Locate every blood parasite and identify its species.
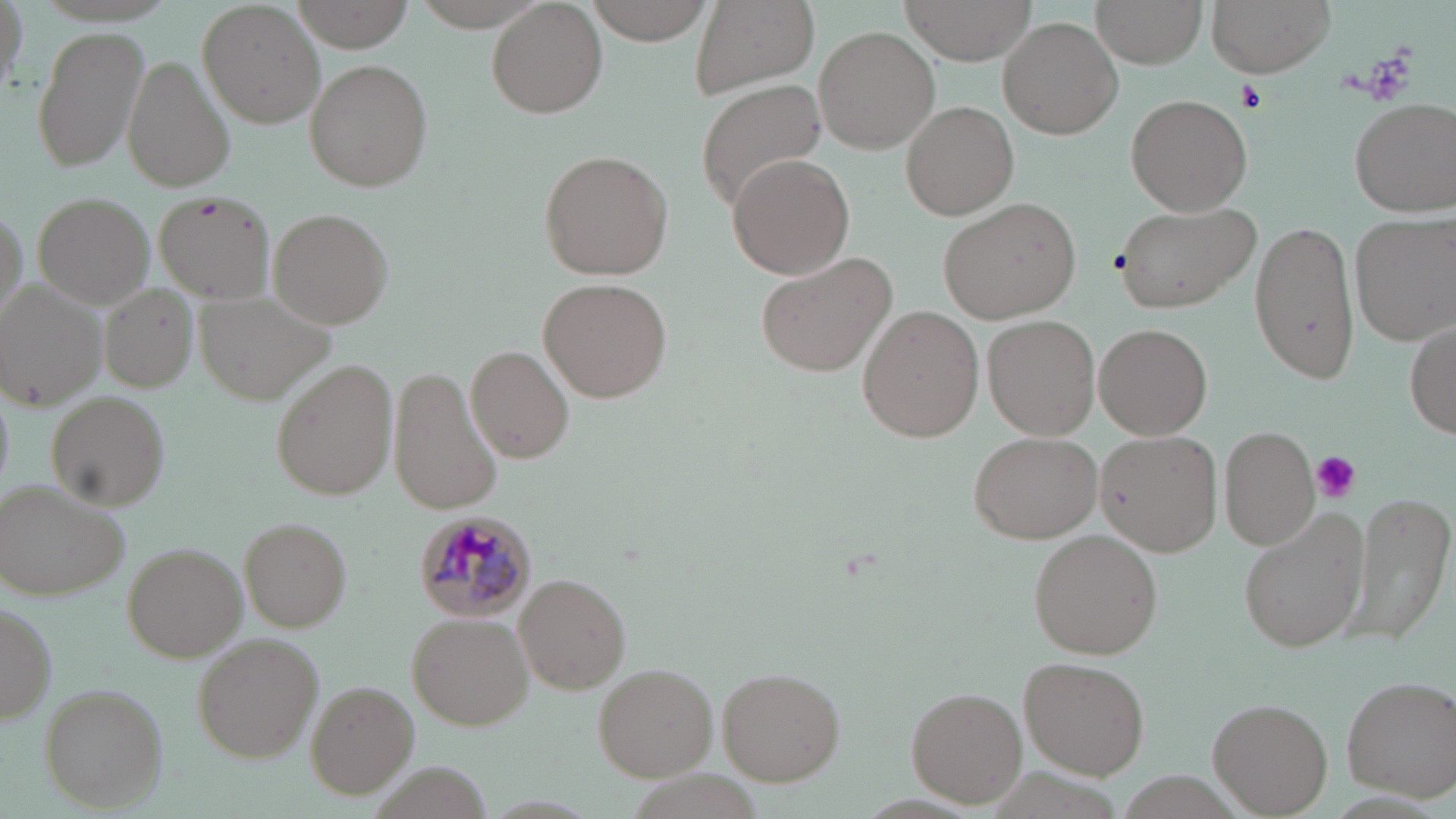
Approximate bounding boxes as (x1, y1, x2, y2) in pixels.
Plasmodium malariae-infected red blood cells: (410, 509, 536, 622).
No Plasmodium falciparum, Plasmodium ovale, Plasmodium vivax, Babesia divergens, or Trypanosoma brucei observed.

Platelet locations: (1237, 79, 1266, 111), (1309, 450, 1361, 502). Uninfected red blood cell locations: (199, 0, 328, 129), (412, 0, 552, 31), (486, 0, 608, 117), (585, 0, 715, 43), (899, 0, 1036, 61), (1092, 0, 1207, 68), (1206, 0, 1334, 76), (0, 1, 27, 98), (689, 1, 820, 97), (291, 2, 409, 52), (998, 15, 1124, 139), (31, 23, 151, 174), (813, 26, 941, 153), (122, 55, 234, 192), (304, 58, 434, 191), (694, 80, 826, 212), (1127, 93, 1252, 215), (1347, 97, 1455, 216), (900, 101, 1018, 220), (538, 147, 674, 281), (726, 153, 854, 280), (155, 190, 278, 304), (31, 191, 155, 310), (939, 196, 1082, 322), (1114, 200, 1260, 312), (267, 207, 394, 329), (1352, 211, 1454, 345), (1247, 215, 1363, 386), (755, 247, 901, 377), (540, 277, 672, 403), (4, 283, 108, 409), (99, 284, 200, 393), (857, 306, 983, 443), (984, 315, 1100, 440), (1405, 322, 1456, 438), (1094, 323, 1214, 440), (465, 345, 576, 464), (273, 358, 398, 500), (387, 365, 502, 518), (45, 392, 170, 512), (1220, 425, 1319, 550), (966, 430, 1102, 544), (1096, 430, 1221, 555), (1, 483, 131, 599), (1347, 488, 1455, 647), (1240, 508, 1368, 651), (239, 517, 352, 631), (1029, 529, 1164, 659), (123, 542, 248, 661), (515, 573, 631, 694), (1, 600, 56, 726), (408, 613, 533, 731), (193, 635, 325, 763), (1021, 654, 1151, 779), (594, 663, 718, 781), (717, 667, 844, 785), (1341, 673, 1454, 799), (306, 679, 423, 799), (39, 683, 168, 812), (907, 688, 1026, 805), (1209, 699, 1331, 816). Slide-level diagnosis: Plasmodium malariae. May-Grünwald-Giemsa stain. Image is 1456×819 pixels. Light microscopy. 1000x magnification. Thin blood smear. One field of a larger specimen.